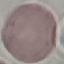 Malaria status: uninfected. Acquired by smartphone through the microscope eyepiece. Giemsa-stained preparation. Cell patch, automatically extracted from a larger field of view and resized to 64 × 64 pixels. Thin blood smear.